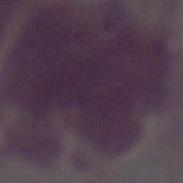
1000x magnification. Photomicrograph. A red blood cell is seen.